Give the position of every malaria parasite.
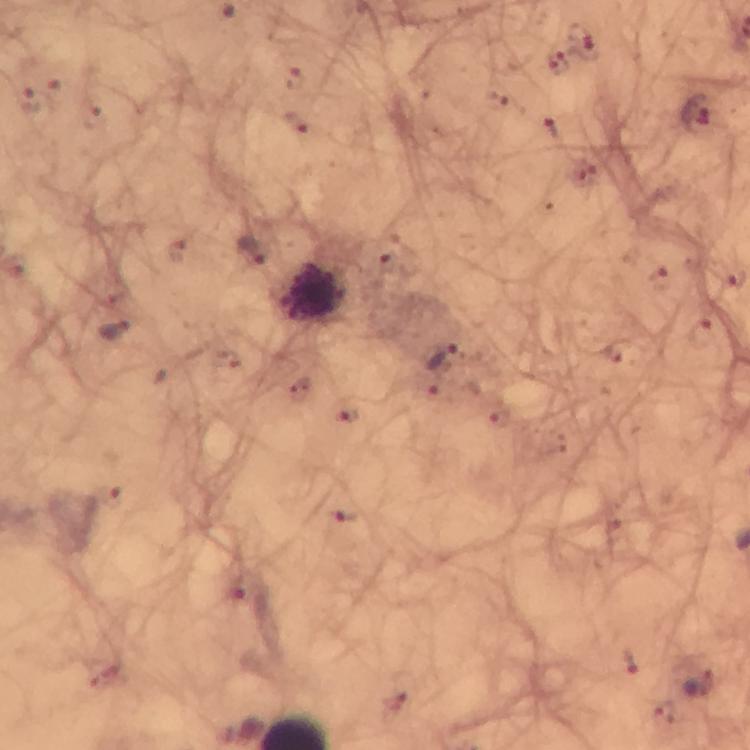
Approximate object centers, in pixels from the top-left corner.
Malaria parasites: (x=585, y=43), (x=556, y=64), (x=296, y=79), (x=54, y=95), (x=28, y=100), (x=699, y=113), (x=297, y=123), (x=553, y=128), (x=253, y=250), (x=116, y=329), (x=700, y=336), (x=612, y=351), (x=443, y=359), (x=344, y=515), (x=631, y=662), (x=700, y=685).

Summary:
  - Leukocyte locations: (x=312, y=293)
  - Magnification: 100x
  - Immersion oil: used
  - Stain: Giemsa
  - Capture: smartphone photograph through a microscope
  - Cropped from: one field of view
  - Image size: 750×750 pixels
  - Context: from a diagnostic examination for malaria
  - Preparation: thick smear